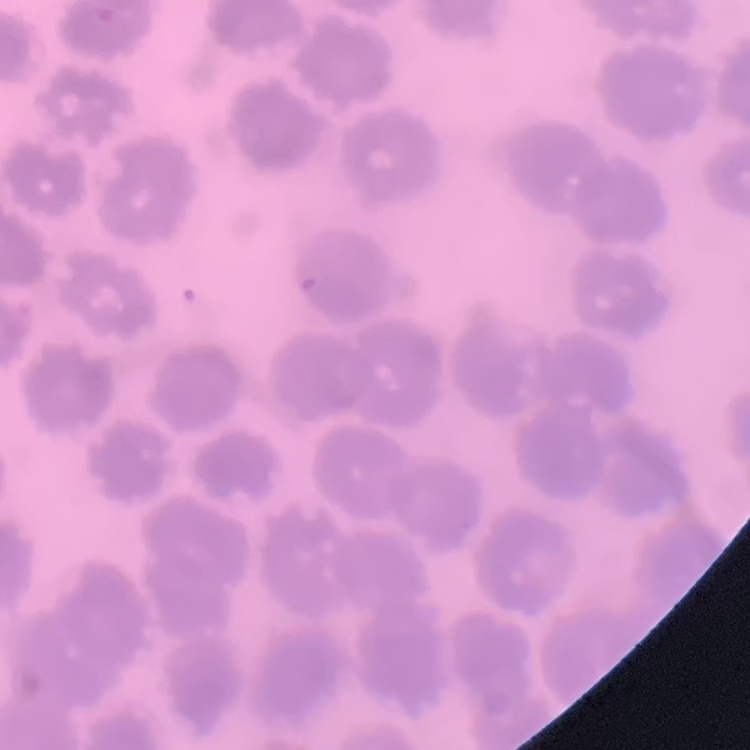

The red blood cells exhibit no rouleaux formation. Square crop of a larger photomicrograph. Thin blood film. Field's or Giemsa stain.